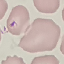
malaria_status: uninfected
image_type: cell patch, automatically extracted from a larger field of view and resized to 64 × 64 pixels
stain: Giemsa
preparation: thin blood smear
capture: smartphone camera at the microscope eyepiece